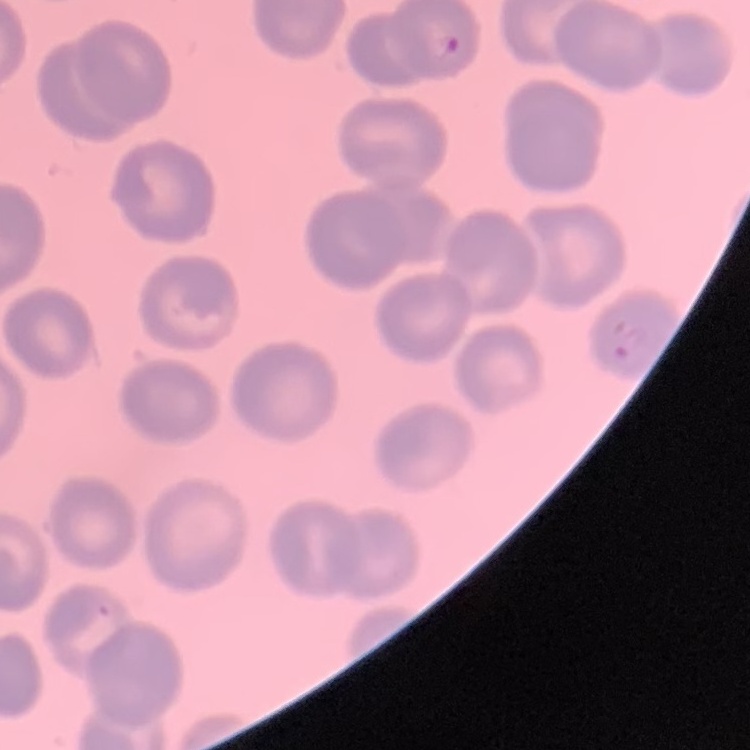

red blood cell morphology = no rouleaux formation
stain = Field's or Giemsa
preparation = thin peripheral smear
image type = one tile cut from a larger photomicrograph